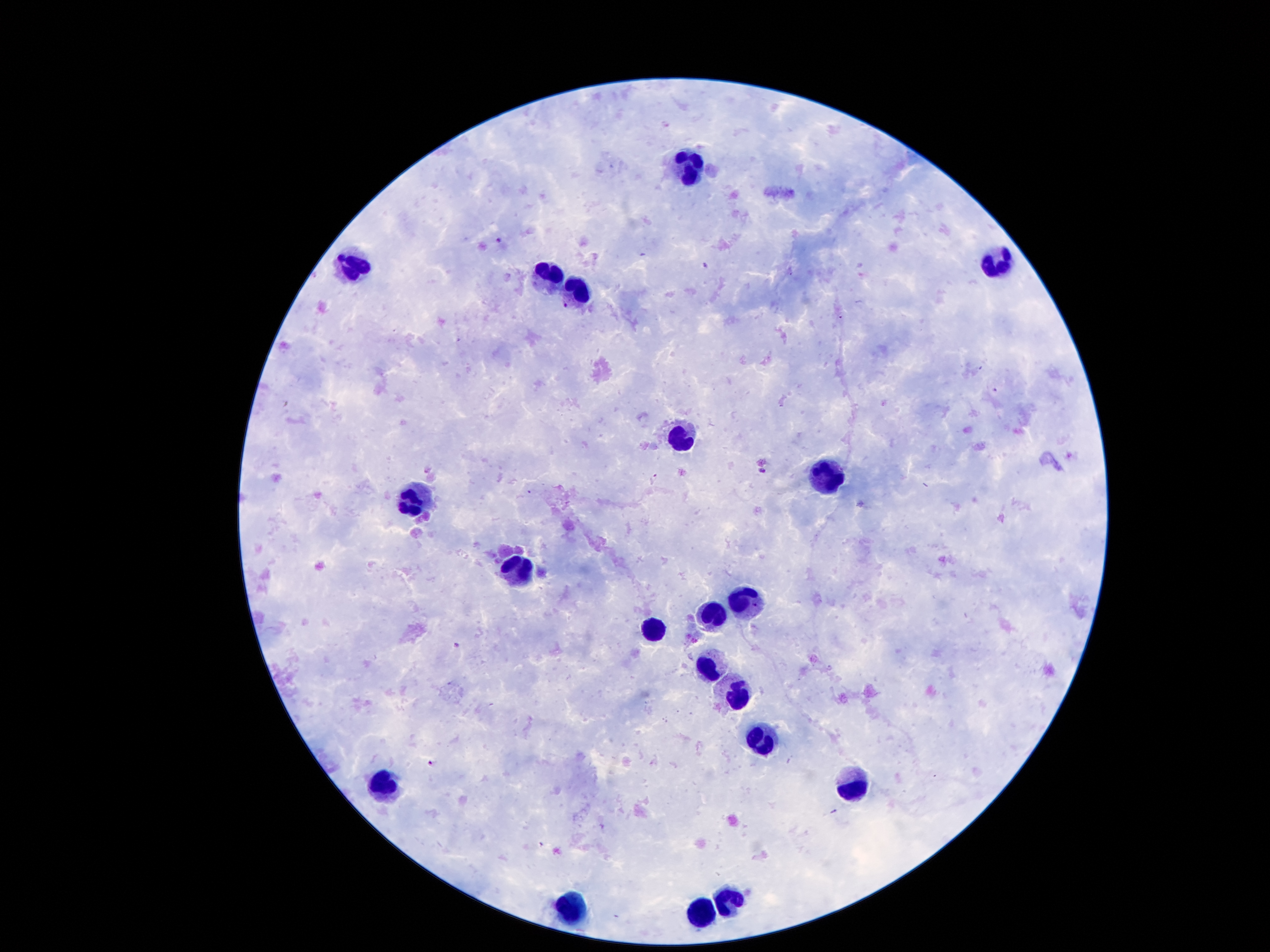 Giemsa-stained preparation. Photographed through the microscope eyepiece with a smartphone camera. Patient malaria status: infected with Plasmodium falciparum. 100x magnification. Single field of view. Thick blood smear. Image is 1270×952 pixels.